Locate every blood parasite and identify its species.
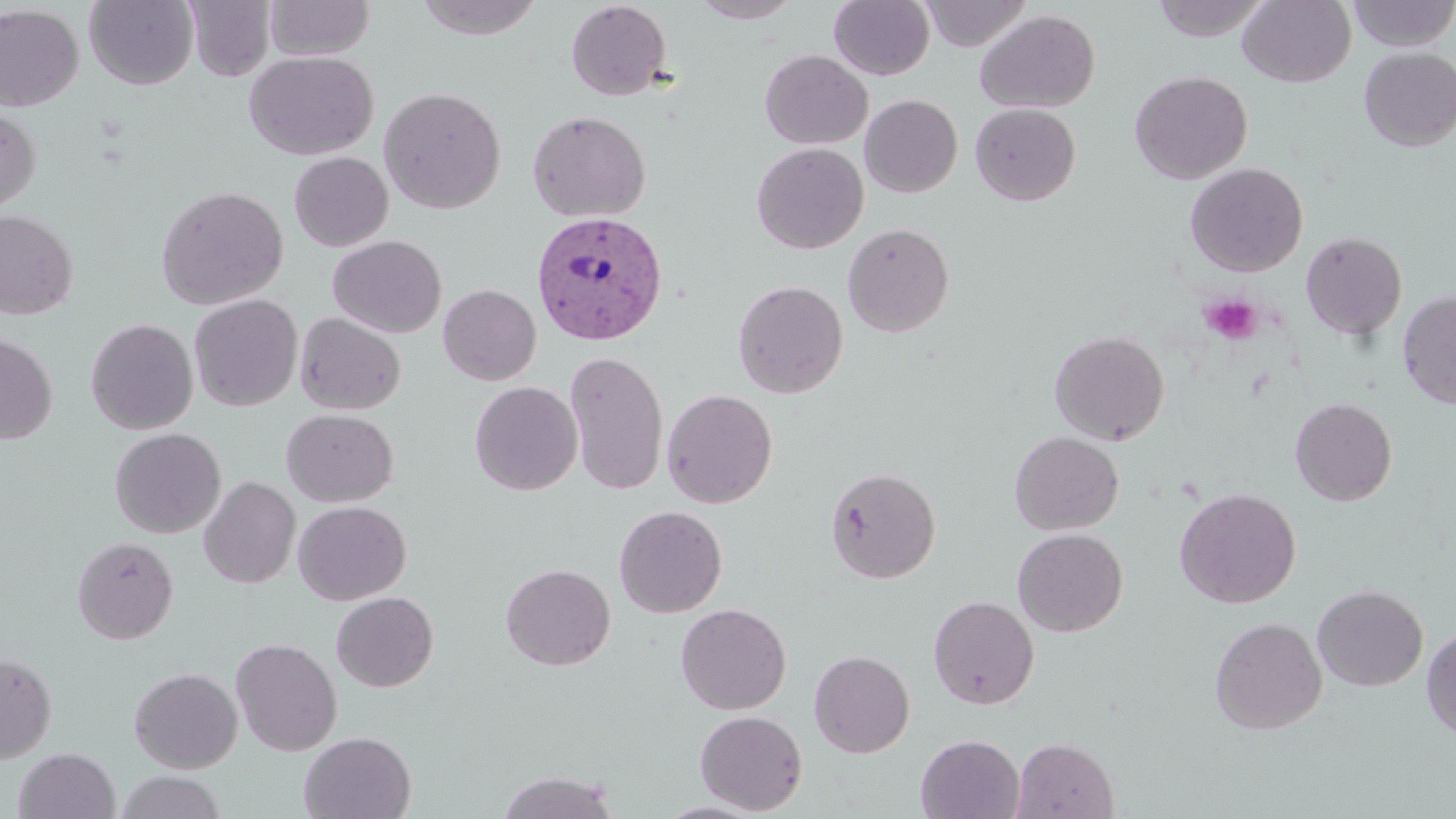
Approximate bounding boxes as named x1/y1/x2/y2 corners in pixels.
Plasmodium vivax-infected red blood cells: (x1=531, y1=209, x2=668, y2=345).
No Plasmodium falciparum, Plasmodium ovale, Plasmodium malariae, Babesia divergens, or Trypanosoma brucei observed.

{
  "slide_level_diagnosis": "Plasmodium vivax",
  "magnification": "1000x",
  "modality": "light microscopy",
  "platelet_locations": "approximate bounding boxes as named x1/y1/x2/y2 corners in pixels: (x1=1200, y1=293, x2=1262, y2=345)",
  "field_of_view": "one of a larger specimen",
  "image_size": "1456×819 pixels",
  "preparation": "thin blood film",
  "uninfected_red_blood_cell_locations": "approximate bounding boxes as named x1/y1/x2/y2 corners in pixels: (x1=84, y1=0, x2=199, y2=90), (x1=185, y1=0, x2=276, y2=81), (x1=264, y1=0, x2=375, y2=60), (x1=413, y1=0, x2=549, y2=41), (x1=689, y1=0, x2=803, y2=23), (x1=829, y1=0, x2=935, y2=80), (x1=920, y1=0, x2=1031, y2=50), (x1=1152, y1=0, x2=1271, y2=42), (x1=1238, y1=0, x2=1356, y2=87), (x1=1347, y1=0, x2=1456, y2=50), (x1=565, y1=1, x2=673, y2=101), (x1=0, y1=4, x2=84, y2=112), (x1=975, y1=9, x2=1100, y2=113), (x1=1358, y1=48, x2=1456, y2=151), (x1=760, y1=49, x2=872, y2=149), (x1=244, y1=50, x2=378, y2=160), (x1=1129, y1=70, x2=1253, y2=184), (x1=378, y1=86, x2=507, y2=214), (x1=860, y1=94, x2=962, y2=198), (x1=970, y1=103, x2=1081, y2=206), (x1=0, y1=107, x2=41, y2=214), (x1=527, y1=110, x2=651, y2=223), (x1=751, y1=142, x2=868, y2=254), (x1=289, y1=152, x2=393, y2=251), (x1=1185, y1=162, x2=1309, y2=277), (x1=155, y1=186, x2=289, y2=310), (x1=0, y1=209, x2=78, y2=320), (x1=842, y1=223, x2=955, y2=337), (x1=1300, y1=231, x2=1407, y2=340), (x1=328, y1=235, x2=447, y2=337), (x1=733, y1=280, x2=848, y2=398), (x1=438, y1=284, x2=541, y2=385), (x1=1397, y1=290, x2=1456, y2=410), (x1=188, y1=294, x2=303, y2=412), (x1=295, y1=312, x2=406, y2=415), (x1=85, y1=318, x2=199, y2=434), (x1=1049, y1=329, x2=1170, y2=445), (x1=0, y1=334, x2=58, y2=445), (x1=565, y1=351, x2=669, y2=495), (x1=469, y1=381, x2=583, y2=495), (x1=661, y1=388, x2=778, y2=508), (x1=1290, y1=397, x2=1397, y2=506), (x1=281, y1=408, x2=398, y2=507), (x1=110, y1=427, x2=226, y2=538), (x1=1009, y1=431, x2=1124, y2=535), (x1=826, y1=466, x2=941, y2=583), (x1=199, y1=476, x2=301, y2=588), (x1=1174, y1=487, x2=1301, y2=608), (x1=293, y1=500, x2=411, y2=605), (x1=613, y1=505, x2=728, y2=618), (x1=1012, y1=528, x2=1128, y2=637), (x1=72, y1=535, x2=179, y2=644), (x1=500, y1=563, x2=615, y2=671), (x1=1312, y1=584, x2=1428, y2=692), (x1=331, y1=591, x2=438, y2=692), (x1=928, y1=595, x2=1039, y2=709), (x1=676, y1=603, x2=791, y2=715), (x1=1209, y1=617, x2=1327, y2=734), (x1=1421, y1=627, x2=1456, y2=741), (x1=230, y1=637, x2=342, y2=755), (x1=809, y1=649, x2=915, y2=758), (x1=0, y1=653, x2=57, y2=763), (x1=129, y1=667, x2=243, y2=773), (x1=694, y1=710, x2=808, y2=814), (x1=299, y1=730, x2=417, y2=819), (x1=915, y1=734, x2=1025, y2=819), (x1=1012, y1=737, x2=1120, y2=819), (x1=13, y1=747, x2=120, y2=819), (x1=496, y1=770, x2=620, y2=818), (x1=116, y1=771, x2=227, y2=819), (x1=654, y1=800, x2=773, y2=818)",
  "stain": "May-Grünwald-Giemsa"
}